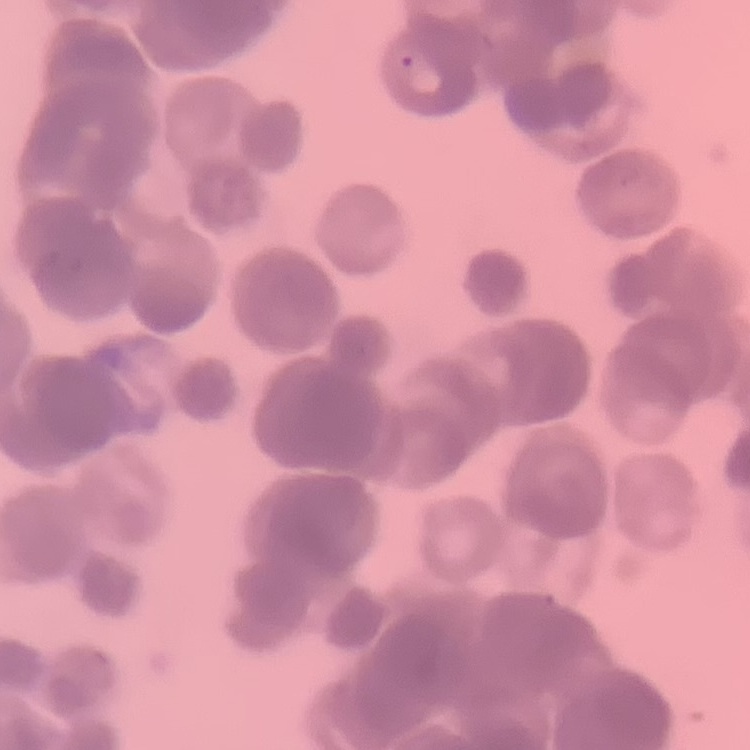

The erythrocytes show rouleaux formation. Square crop of a larger photomicrograph. Stained with either Field's or Giemsa. Thin peripheral smear.